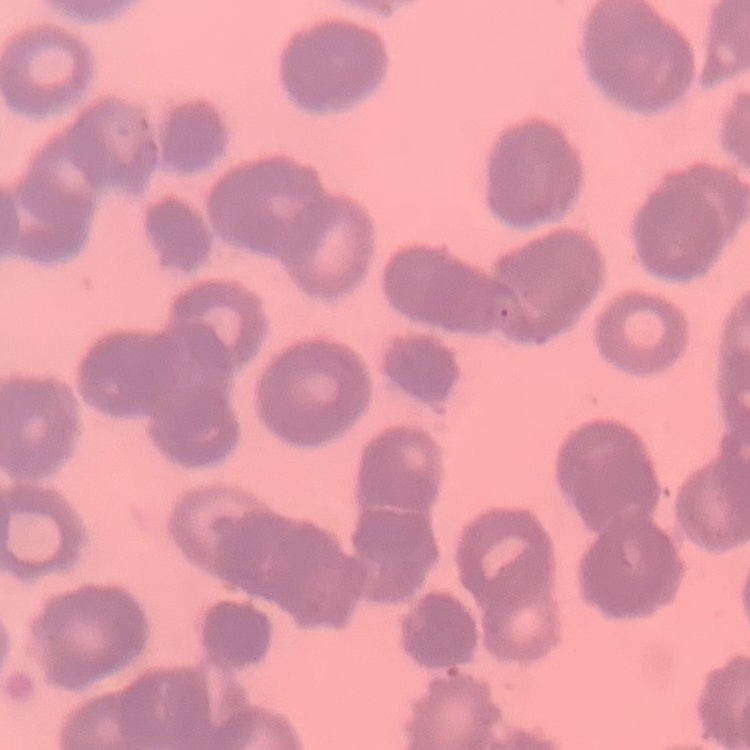
{
  "red_blood_cell_morphology": "rouleaux formation",
  "preparation": "thin peripheral smear",
  "stain": "Field's or Giemsa",
  "image_type": "square crop of a larger photomicrograph"
}